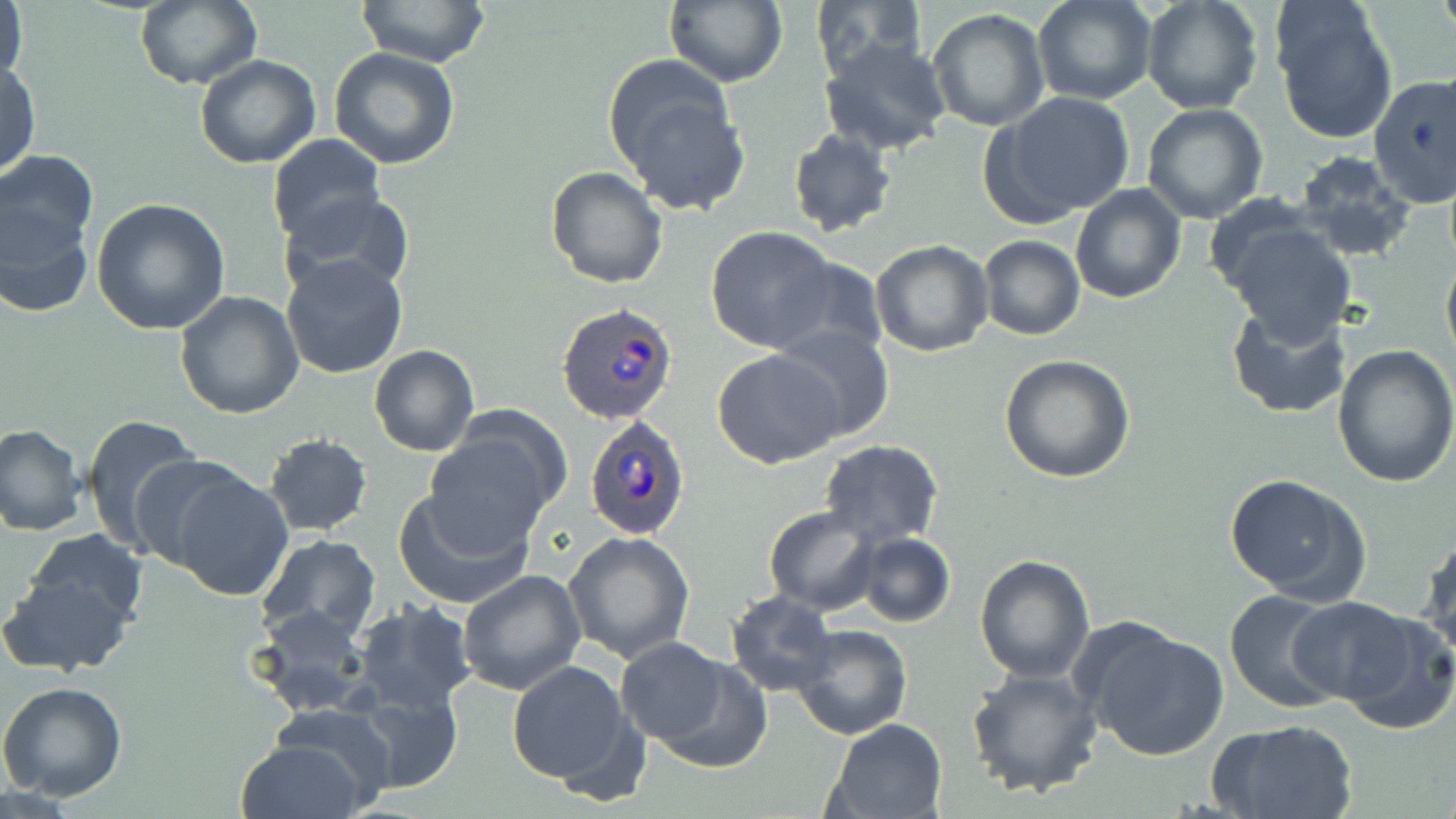
Approximate bounding boxes as (x1, y1, x2, y2) in pixels. Plasmodium ovale-infected red blood cell locations: (555, 303, 678, 427), (585, 416, 691, 539). Uninfected red blood cell locations: (1, 0, 28, 92), (663, 0, 786, 89), (810, 0, 923, 78), (1032, 0, 1157, 107), (1139, 0, 1265, 115), (1271, 0, 1398, 146), (358, 1, 490, 68), (133, 2, 262, 89), (926, 9, 1049, 131), (819, 36, 951, 157), (328, 48, 459, 170), (194, 55, 322, 169), (602, 57, 751, 216), (1, 59, 41, 179), (1368, 73, 1456, 209), (985, 91, 1136, 225), (1142, 103, 1269, 224), (787, 127, 899, 239), (266, 134, 385, 246), (1293, 153, 1416, 260), (0, 157, 95, 303), (545, 166, 668, 289), (1069, 183, 1187, 304), (284, 192, 415, 298), (90, 199, 230, 334), (1223, 221, 1356, 343), (704, 226, 840, 354), (979, 236, 1085, 340), (870, 239, 994, 357), (1441, 251, 1456, 372), (281, 254, 409, 380), (772, 257, 888, 362), (174, 291, 305, 420), (1226, 303, 1353, 420), (770, 325, 895, 444), (368, 345, 480, 458), (1331, 345, 1456, 487), (712, 349, 842, 468), (999, 354, 1136, 484), (80, 412, 205, 554), (424, 420, 563, 546), (0, 423, 88, 536), (264, 433, 372, 537), (819, 439, 943, 547), (128, 454, 254, 572), (162, 466, 294, 601), (1225, 475, 1370, 604), (392, 485, 537, 609), (763, 507, 879, 615), (24, 529, 146, 630), (563, 531, 695, 663), (1419, 532, 1455, 666), (255, 533, 383, 644), (854, 533, 955, 628), (974, 554, 1094, 684), (458, 568, 585, 696), (0, 573, 135, 678), (1224, 589, 1346, 713), (726, 591, 839, 695), (1286, 597, 1425, 709), (351, 600, 475, 712), (252, 605, 372, 715), (1081, 622, 1231, 760), (788, 623, 912, 739), (613, 640, 736, 747), (640, 651, 774, 775), (505, 660, 639, 787), (965, 668, 1103, 797), (345, 679, 465, 792), (0, 682, 128, 803), (266, 704, 400, 810), (1210, 717, 1360, 819), (821, 718, 950, 819), (234, 738, 369, 819). Slide-level diagnosis: Plasmodium ovale. Light microscopy. Image is 1456×819 pixels. One field of a larger specimen. May-Grünwald-Giemsa stain. 1000x magnification. Thin blood smear.